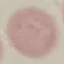
Summary:
  - Malaria status: uninfected
  - Preparation: thin blood smear
  - Capture: smartphone through the microscope eyepiece
  - Stain: Giemsa
  - Image type: cell patch, automatically extracted from a larger field of view and resized to 64 × 64 pixels